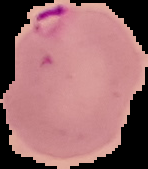

Summary:
  - Preparation: thin blood film
  - Image size: 148×169 pixels
  - Malaria status: parasitized
  - Image type: segmented cell region on a black background